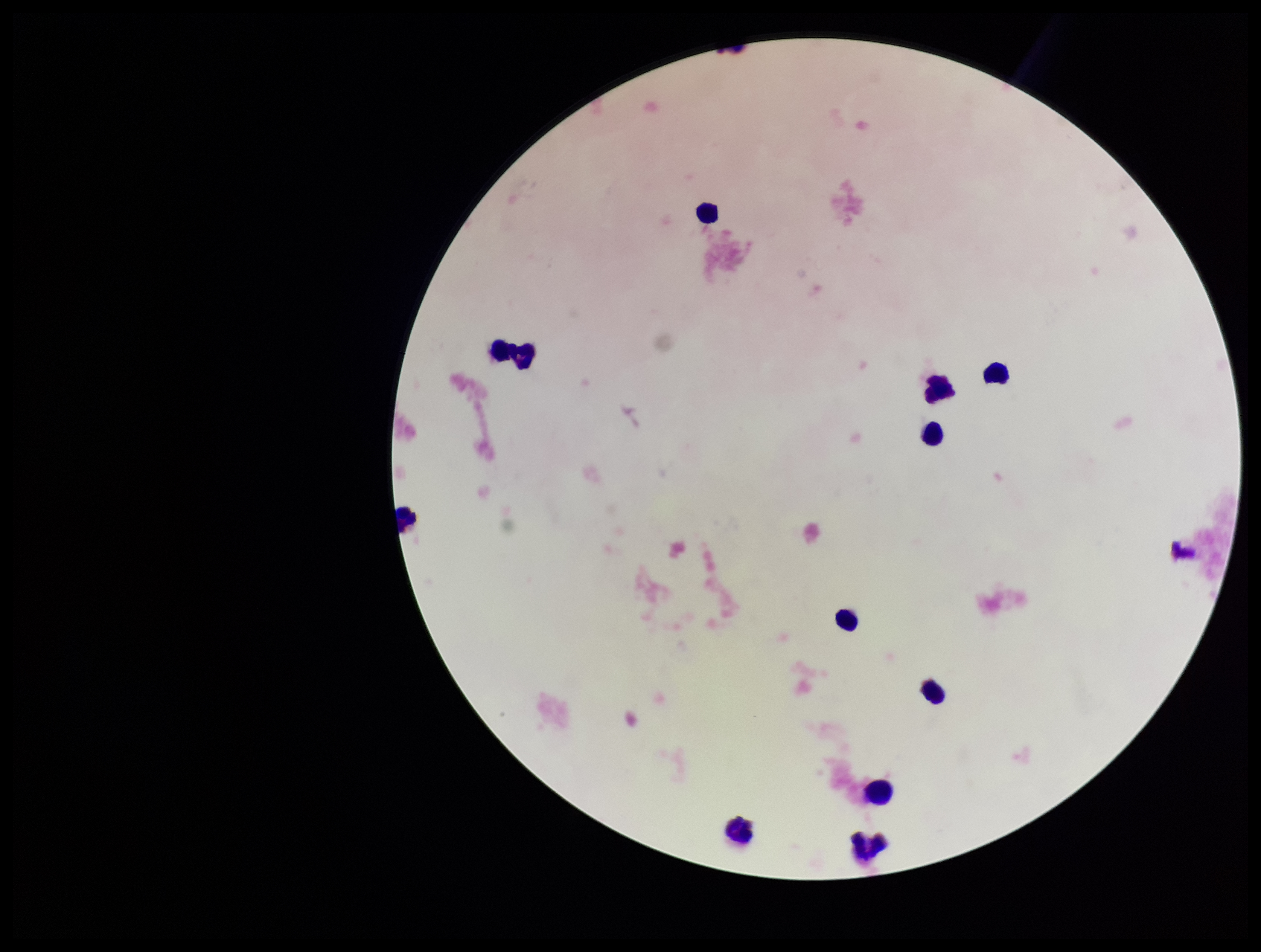

Plasmodium parasites = none identified
image size = 1261×952 pixels
leukocyte count = 11
parasite count = 0
patient malaria status = negative
preparation = thick smear
capture = smartphone photograph through the microscope eyepiece
field of view = single
stain = Giemsa